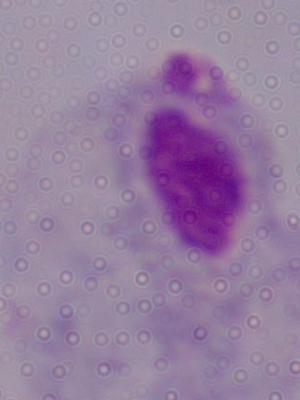
{
  "modality": "micrograph",
  "identification": "trichomonad",
  "magnification": "1000x"
}